Classify this cell by malaria status.
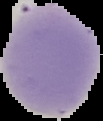

Uninfected.

Summary:
  - Image size: 103×121 pixels
  - Preparation: thin blood smear
  - Image type: segmented cell region on a black background